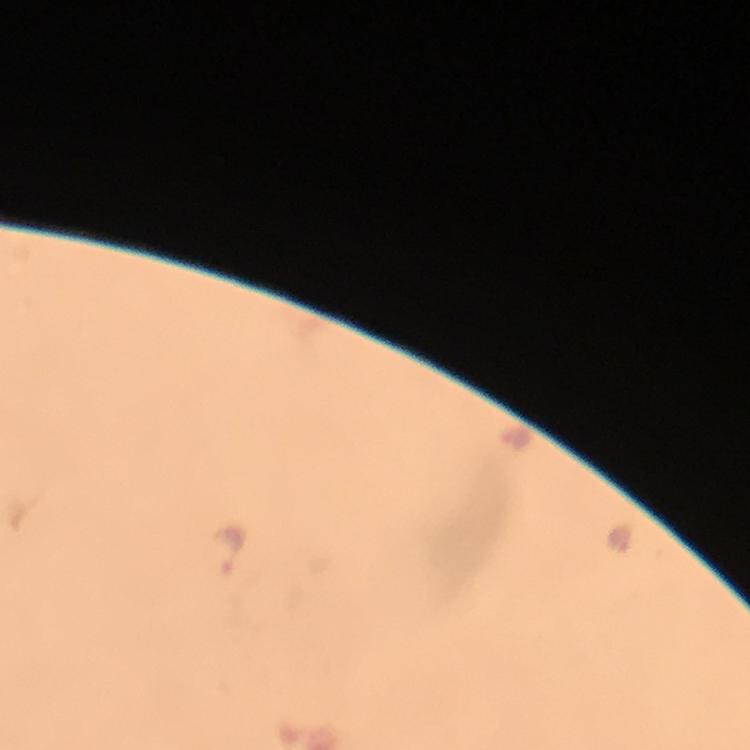

Approximate centers as [x, y] in pixels.
Summary:
  - Plasmodium parasite locations: [512, 437], [227, 548]
  - Stain: Giemsa
  - Immersion oil: used
  - Image size: 750×750 pixels
  - Magnification: 100x
  - Cropped from: one field of view
  - Capture: smartphone mounted on the microscope
  - Preparation: thick smear
  - Context: from a diagnostic examination for malaria